State which cell type is depicted.
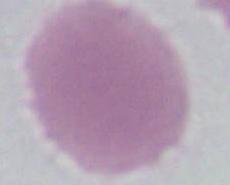

An erythrocyte.

Summary:
  - Modality: micrograph
  - Magnification: 1000x